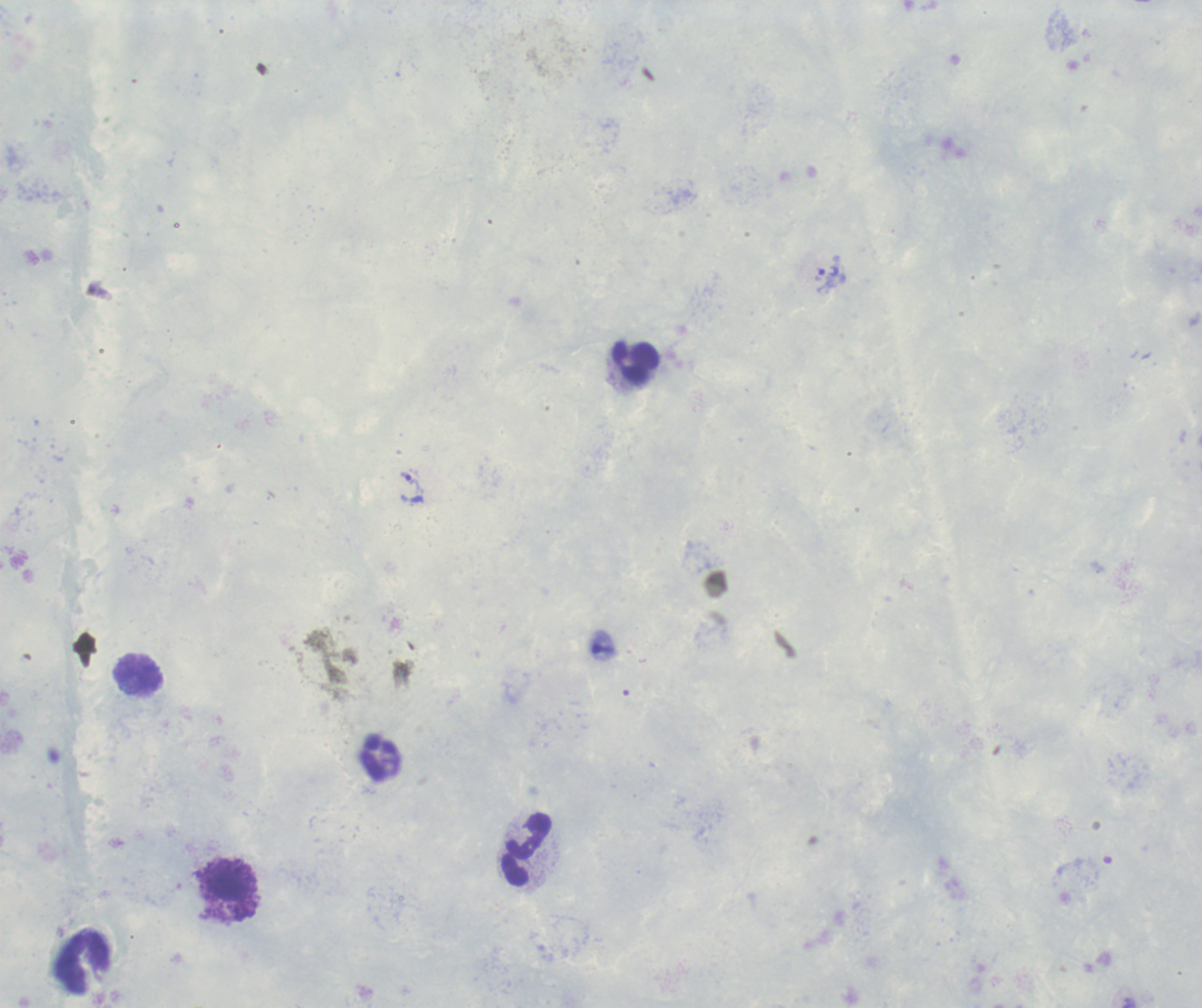

coordinate format = approximate object centers, in pixels from the top-left corner
trophozoite locations = (x=829, y=274), (x=409, y=481)
leukocyte locations = (x=636, y=364), (x=138, y=675), (x=528, y=851), (x=230, y=890), (x=84, y=962)
stain = Romanowsky
coloration quality = good
field of view = single
magnification = 100x
image size = 1202×1008 pixels
context = previously used in a real diagnosis
preparation = thick blood smear
result = positive for malaria parasites
background quality = unsatisfactory